State which parasite is depicted.
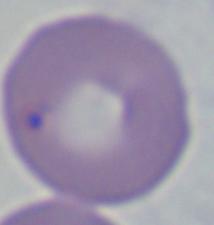

This is Babesia.

modality = micrograph
magnification = 1000x